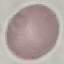

Summary:
  - Result: negative for malaria parasites
  - Image type: cell patch, automatically extracted from a larger field of view and resized to 64 × 64 pixels
  - Stain: Giemsa
  - Capture: smartphone through the microscope eyepiece
  - Preparation: thin blood smear